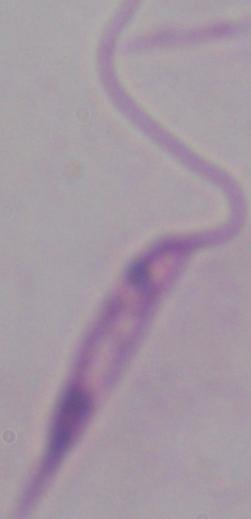

Photomicrograph. Captured at 1000x magnification. A Leishmania parasite is seen.